Describe the morphology of the erythrocytes.
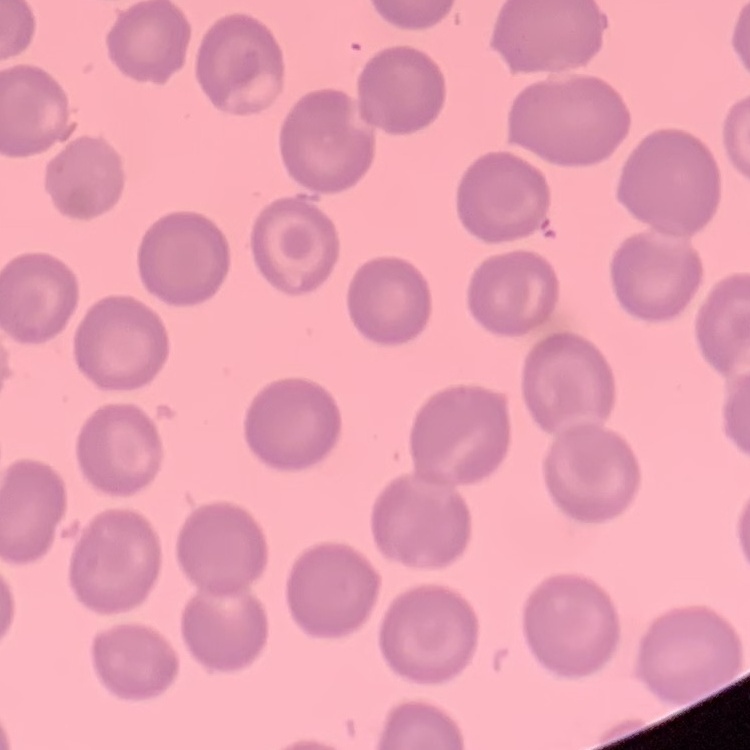

They show no rouleaux formation.

Thin peripheral smear. One tile cut from a larger photomicrograph. Stained with either Field's or Giemsa.